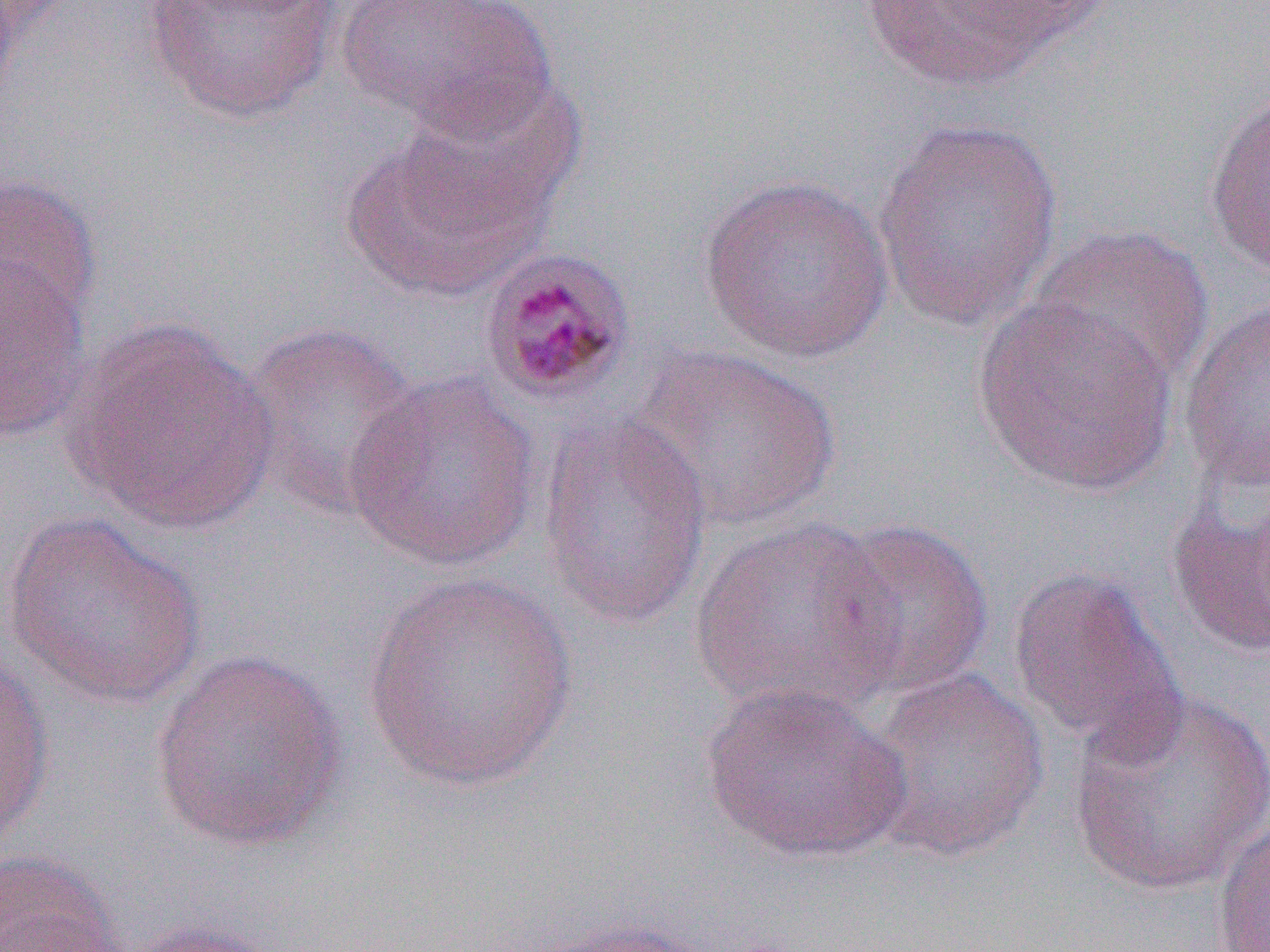

slide-level diagnosis = Plasmodium malariae
magnification = 1000x
modality = optical microscopy
preparation = thin blood smear
field of view = one of a larger specimen
Plasmodium malariae-infected red blood cell locations = approximate bounding boxes as (x1,y1)-(x2,y2) corner pairs in pixels: (476,245)-(638,407)
image size = 1270×952 pixels
uninfected red blood cell locations = approximate bounding boxes as (x1,y1)-(x2,y2) corner pairs in pixels: (141,0)-(344,124), (337,0)-(557,140), (849,0)-(1105,93), (400,76)-(586,234), (1202,90)-(1270,281), (872,114)-(1066,336), (339,126)-(550,302), (0,173)-(102,336), (698,173)-(895,364), (1027,224)-(1214,391), (0,255)-(93,441), (971,296)-(1178,497), (1178,296)-(1270,491), (66,321)-(278,535), (237,321)-(424,521), (629,344)-(841,534), (341,370)-(543,574), (537,413)-(713,630), (1166,462)-(1270,662), (1,512)-(207,709), (690,516)-(903,720), (822,517)-(994,700), (1005,565)-(1180,752), (359,573)-(579,792), (0,650)-(54,851), (148,651)-(348,854), (859,666)-(1050,864), (697,680)-(911,865), (1068,686)-(1270,899), (1212,815)-(1270,952), (0,849)-(132,952), (523,916)-(719,951), (120,919)-(289,951)